Outline each uninfected red blood cell.
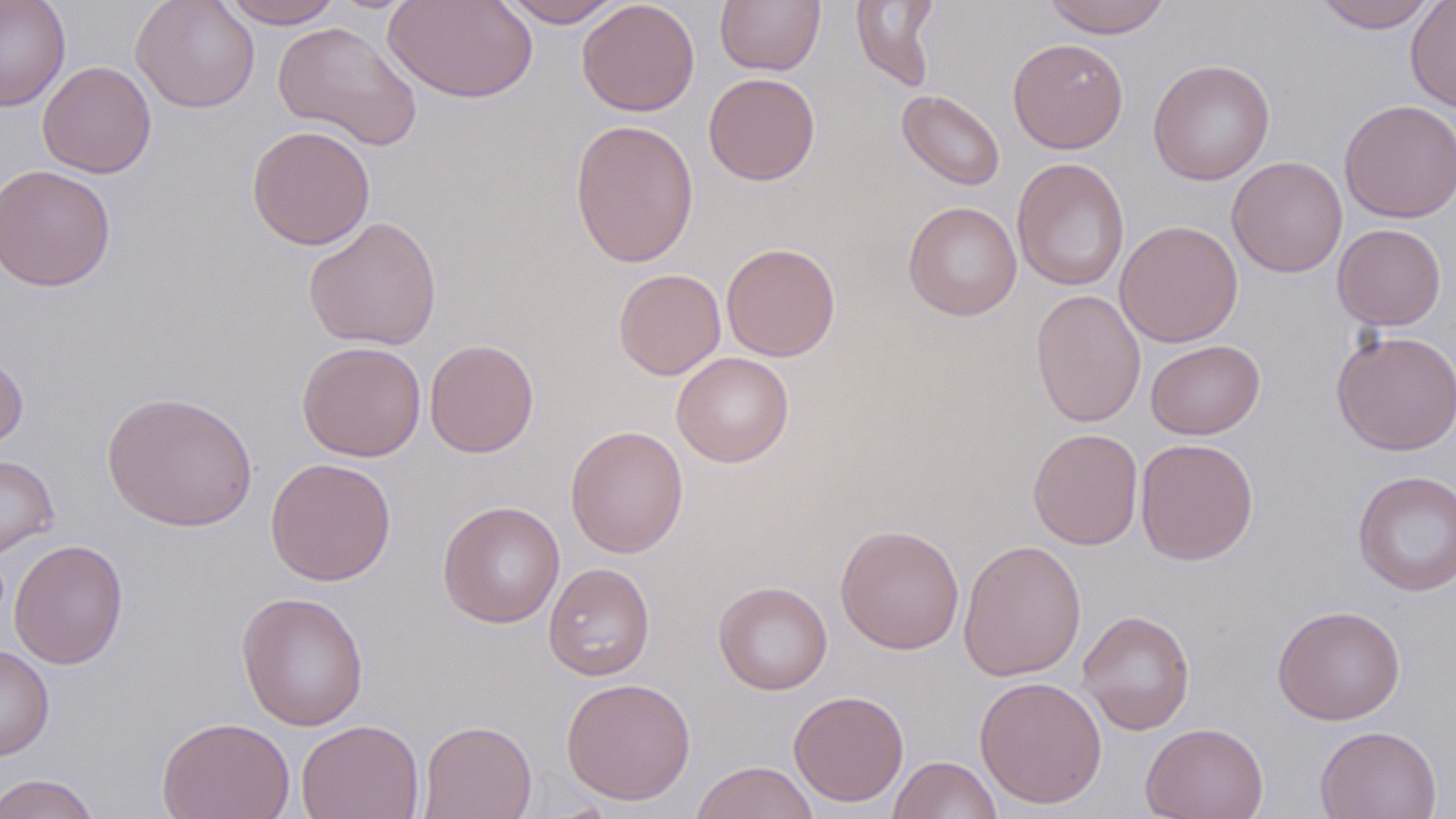

Approximate bounding boxes as named x1/y1/x2/y2 corners in pixels.
Uninfected red blood cells: (x1=0, y1=0, x2=71, y2=112), (x1=131, y1=0, x2=260, y2=113), (x1=218, y1=0, x2=343, y2=28), (x1=382, y1=0, x2=538, y2=104), (x1=498, y1=0, x2=625, y2=27), (x1=576, y1=0, x2=700, y2=116), (x1=715, y1=0, x2=825, y2=76), (x1=1042, y1=0, x2=1172, y2=38), (x1=1312, y1=0, x2=1440, y2=33), (x1=1405, y1=0, x2=1456, y2=113), (x1=850, y1=1, x2=941, y2=91), (x1=273, y1=21, x2=422, y2=151), (x1=1007, y1=38, x2=1128, y2=153), (x1=1148, y1=59, x2=1275, y2=185), (x1=37, y1=60, x2=157, y2=178), (x1=703, y1=72, x2=820, y2=185), (x1=897, y1=89, x2=1005, y2=191), (x1=1338, y1=99, x2=1456, y2=223), (x1=569, y1=118, x2=699, y2=269), (x1=246, y1=125, x2=375, y2=250), (x1=1226, y1=157, x2=1347, y2=277), (x1=1011, y1=158, x2=1130, y2=292), (x1=0, y1=164, x2=116, y2=291), (x1=903, y1=201, x2=1022, y2=321), (x1=303, y1=215, x2=442, y2=351), (x1=1114, y1=220, x2=1243, y2=348), (x1=1333, y1=223, x2=1447, y2=330), (x1=721, y1=242, x2=840, y2=361), (x1=613, y1=268, x2=726, y2=380), (x1=1030, y1=288, x2=1146, y2=428), (x1=1330, y1=330, x2=1456, y2=455), (x1=424, y1=339, x2=539, y2=457), (x1=1145, y1=339, x2=1265, y2=440), (x1=296, y1=340, x2=427, y2=462), (x1=0, y1=349, x2=29, y2=450), (x1=671, y1=352, x2=794, y2=467), (x1=101, y1=390, x2=258, y2=531), (x1=565, y1=425, x2=689, y2=558), (x1=1027, y1=428, x2=1143, y2=550), (x1=1134, y1=438, x2=1259, y2=565), (x1=0, y1=454, x2=59, y2=559), (x1=265, y1=457, x2=396, y2=585), (x1=1352, y1=469, x2=1456, y2=596), (x1=437, y1=501, x2=566, y2=628), (x1=834, y1=524, x2=965, y2=655), (x1=9, y1=539, x2=128, y2=669), (x1=958, y1=539, x2=1087, y2=682), (x1=543, y1=561, x2=655, y2=680), (x1=713, y1=580, x2=832, y2=695), (x1=236, y1=591, x2=369, y2=731), (x1=1272, y1=604, x2=1405, y2=725), (x1=1077, y1=609, x2=1195, y2=735), (x1=0, y1=644, x2=54, y2=760), (x1=974, y1=675, x2=1107, y2=808), (x1=561, y1=677, x2=696, y2=805), (x1=788, y1=690, x2=909, y2=807), (x1=157, y1=715, x2=295, y2=819), (x1=296, y1=719, x2=424, y2=819), (x1=418, y1=719, x2=537, y2=819), (x1=1140, y1=722, x2=1269, y2=819), (x1=1314, y1=725, x2=1443, y2=819), (x1=888, y1=755, x2=1002, y2=819), (x1=689, y1=760, x2=820, y2=819), (x1=1, y1=773, x2=101, y2=819).

Summary:
  - Slide-level diagnosis: negative for blood parasites
  - Stain: May-Grünwald-Giemsa
  - Preparation: thin blood smear
  - Modality: light microscopy
  - Magnification: 1000x
  - Field of view: single
  - Image size: 1456×819 pixels